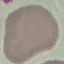
Summary:
  - Malaria status: uninfected
  - Image type: cell patch, automatically extracted from a larger field of view and resized to 64 × 64 pixels
  - Stain: Giemsa
  - Capture: smartphone camera at the microscope eyepiece
  - Preparation: thin smear